Identify the parasite.
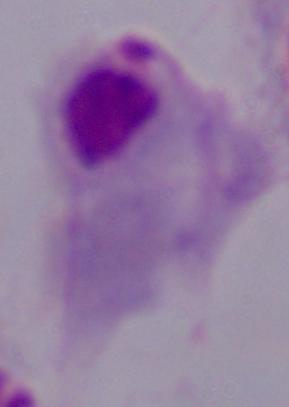
A trichomonad.

modality: micrograph
magnification: 1000x